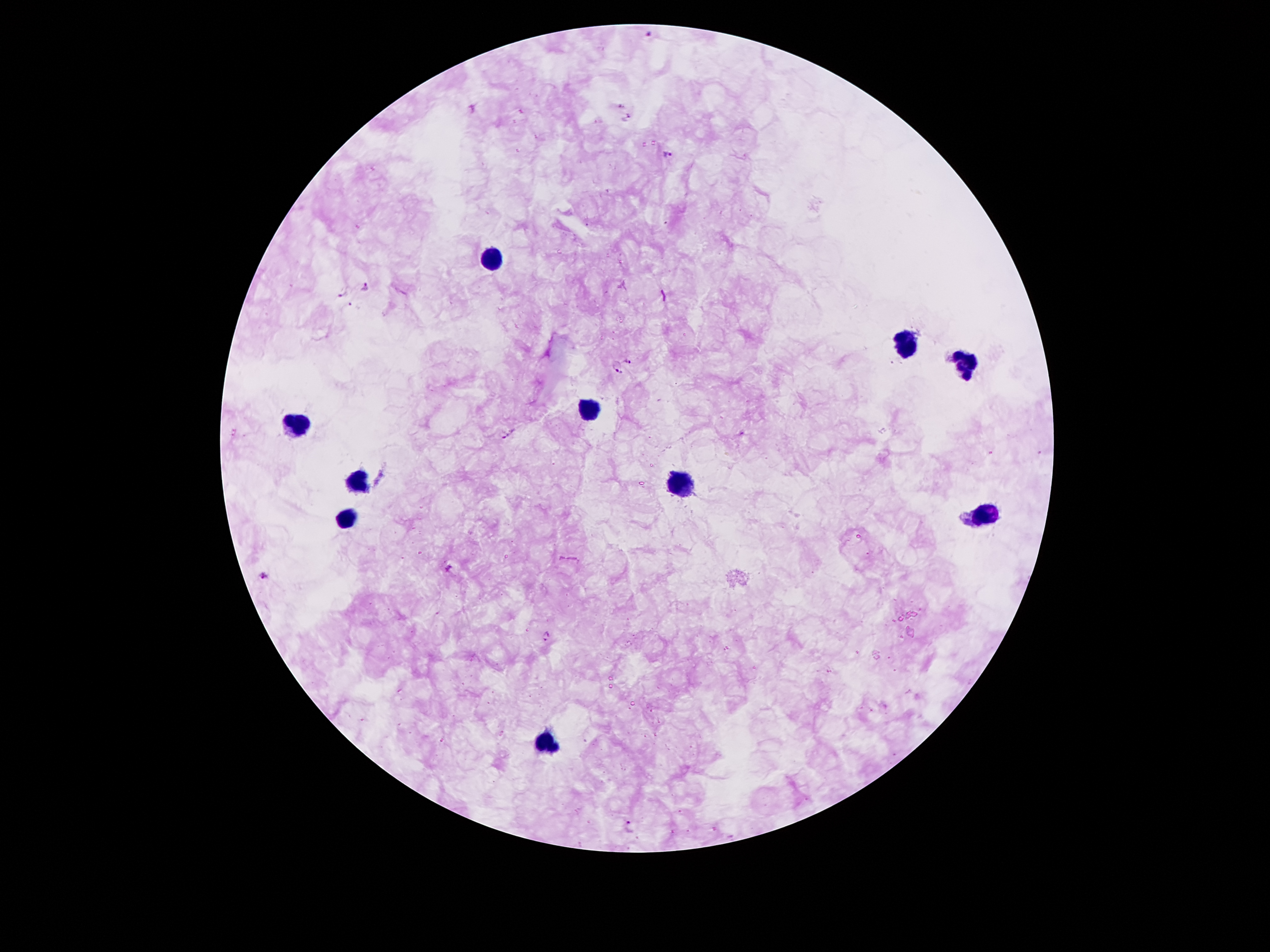
Patient malaria status: positive for Plasmodium falciparum. Smartphone photograph taken through the microscope eyepiece. One field from this slide. Thick peripheral-blood smear. 100x magnification. Giemsa stain. Image is 1270×952 pixels.